Identify the cell.
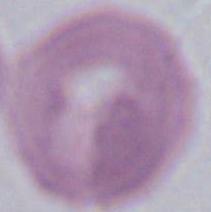
This is an erythrocyte.

Micrograph. Captured at 1000x magnification.